Assess this cell for malaria.
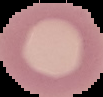

Uninfected.

image type = segmented cell region on a black background
image size = 103×97 pixels
preparation = thin blood smear